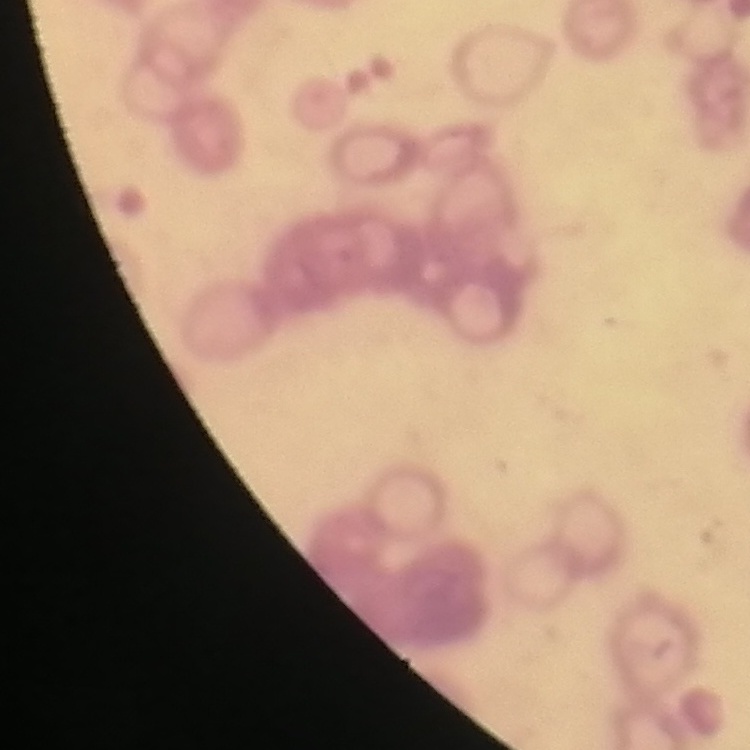

red blood cell morphology = rouleaux formation
image type = one tile cut from a larger photomicrograph
stain = Field's or Giemsa
preparation = thin peripheral smear